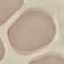
Summary:
  - Result: no malaria parasites detected
  - Preparation: thin blood smear
  - Image type: cell patch, automatically extracted from a larger field of view and resized to 64 × 64 pixels
  - Capture: smartphone camera at the microscope eyepiece
  - Stain: Giemsa